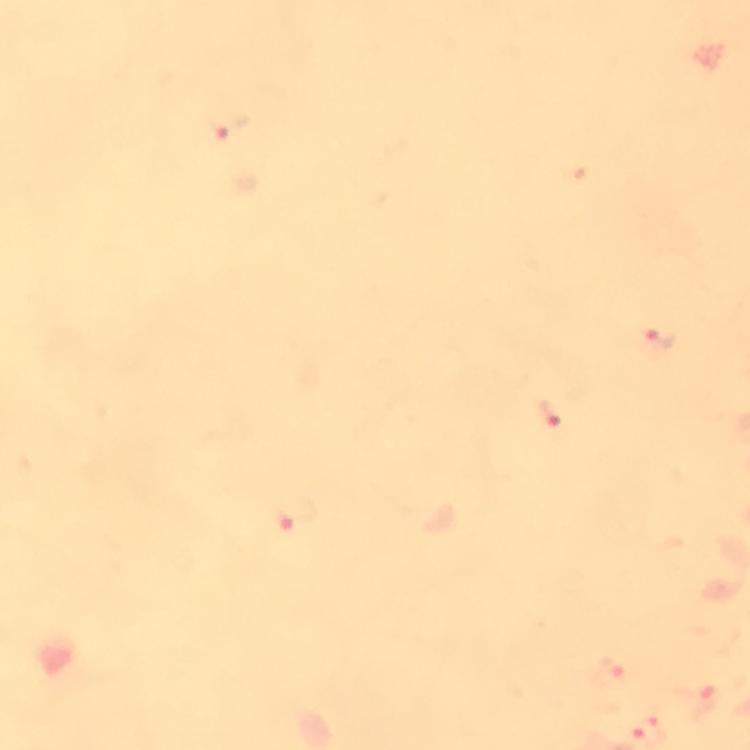
Approximate centers as [x, y] in pixels. Plasmodium parasite locations: [231, 127], [661, 334], [549, 411], [297, 513], [611, 671]. Giemsa-stained preparation. From a malaria diagnostic workup. Immersion oil applied. Image is 750×750 pixels. Photographed through the microscope with a smartphone camera. A crop from one field of view. Thick smear. At 100x magnification.